Classify this cell by malaria status.
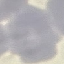
It is uninfected.

image type = automatically extracted cell patch, resized to 64 × 64 pixels
preparation = thin blood smear
stain = Giemsa
capture = smartphone through the microscope eyepiece